Report the malaria status of this cell.
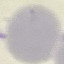

Uninfected.

Acquired by smartphone through the microscope eyepiece. Automatically extracted cell patch, resized to 64 × 64 pixels. Giemsa-stained preparation. Thin blood smear.